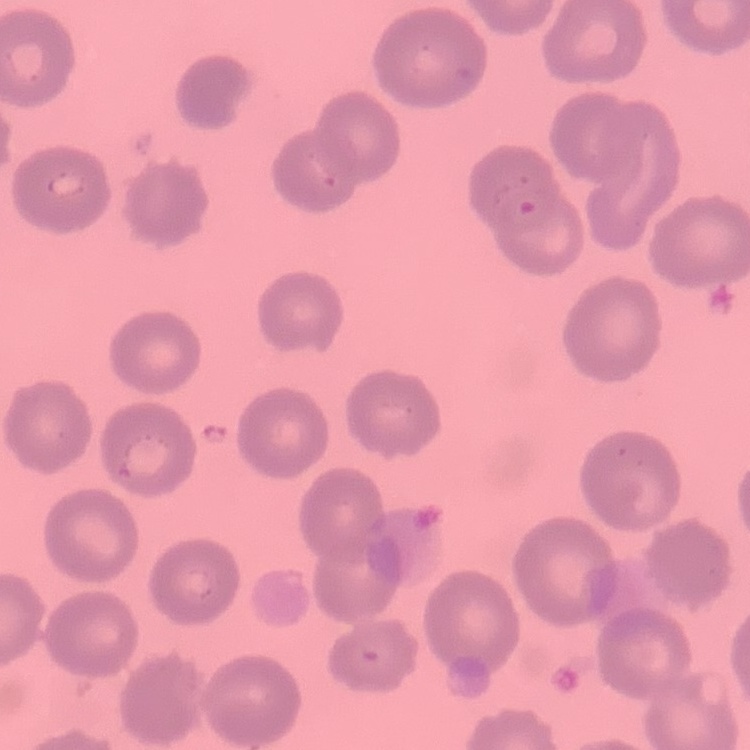
{
  "red_blood_cell_morphology": "no rouleaux formation",
  "preparation": "thin peripheral smear",
  "stain": "Field's or Giemsa",
  "image_type": "square crop of a larger photomicrograph"
}